Outline each blood parasite and name the species.
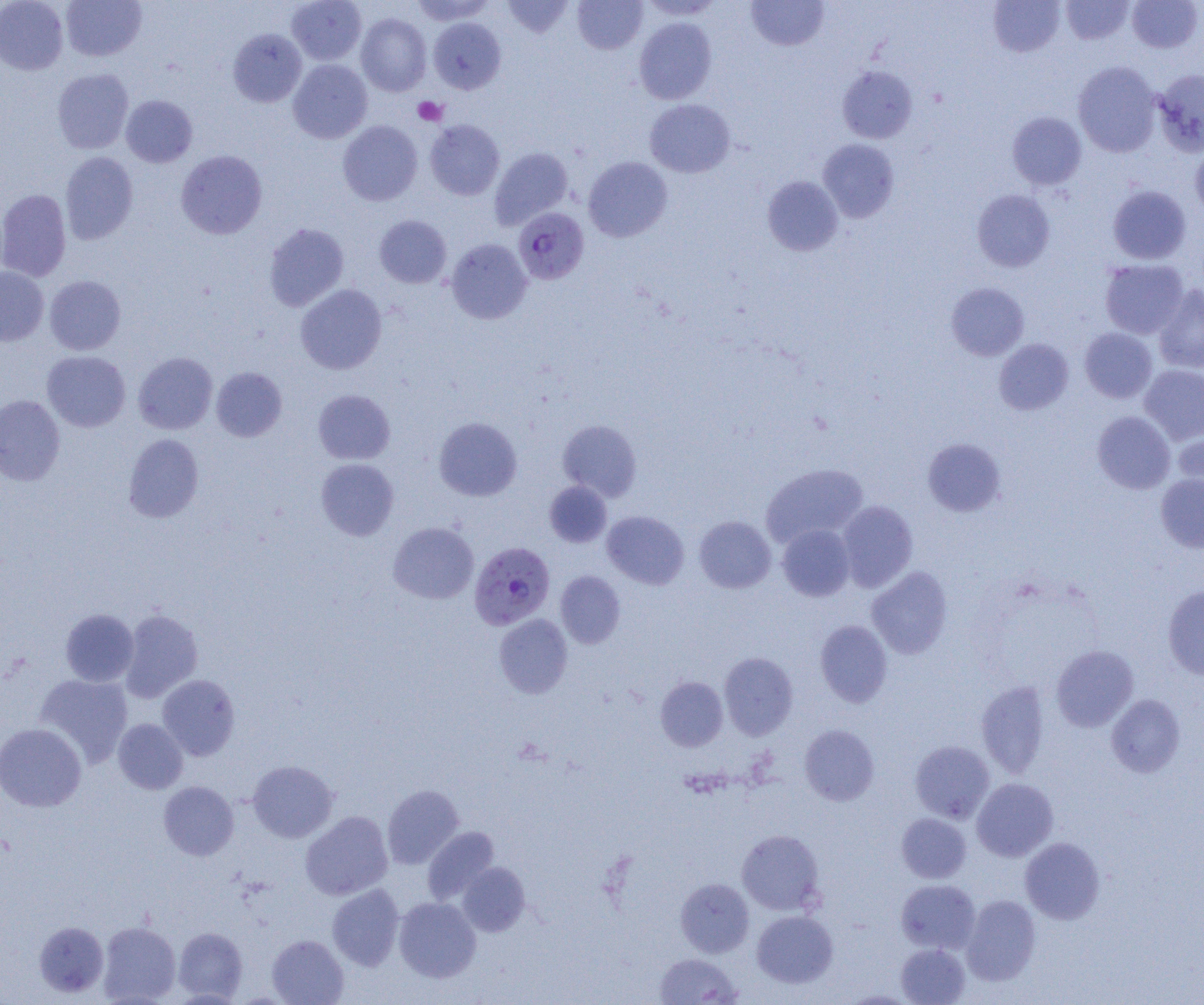
Approximate bounding boxes as (x1, y1, x2, y2) in pixels.
Plasmodium falciparum-infected red blood cells: (513, 208, 589, 285), (469, 542, 555, 629).
No Plasmodium ovale, Plasmodium malariae, Plasmodium vivax, Babesia divergens, or Trypanosoma brucei observed.

slide_level_diagnosis: Plasmodium falciparum
preparation: thin blood smear
magnification: 1000x
platelet_locations: 'approximate bounding boxes as (x1, y1, x2, y2) in pixels: (413, 96, 447, 126)'
modality: light microscopy
field_of_view: one of a larger specimen
image_size: 1204×1005 pixels
uninfected_red_blood_cell_locations: 'approximate bounding boxes as (x1, y1, x2, y2) in pixels: (0, 0, 68, 75), (61, 0, 147, 61), (287, 0, 366, 65), (410, 0, 495, 25), (502, 0, 573, 39), (573, 0, 647, 54), (639, 0, 723, 20), (746, 0, 828, 51), (988, 0, 1065, 58), (1127, 0, 1202, 52), (1061, 1, 1134, 44), (356, 13, 432, 96), (634, 16, 716, 105), (428, 17, 505, 94), (228, 28, 307, 107), (288, 59, 372, 143), (1072, 61, 1162, 157), (837, 66, 917, 144), (53, 68, 133, 154), (1154, 68, 1204, 156), (121, 95, 197, 167), (645, 99, 735, 178), (1007, 111, 1086, 190), (425, 119, 504, 200), (338, 120, 423, 206), (818, 139, 899, 222), (1190, 143, 1204, 220), (489, 147, 573, 230), (176, 150, 267, 239), (60, 152, 138, 244), (583, 156, 672, 242), (762, 176, 843, 256), (1107, 185, 1191, 264), (0, 189, 71, 282), (972, 189, 1055, 272), (374, 215, 451, 288), (264, 223, 349, 311), (445, 238, 532, 324), (1100, 259, 1188, 339), (0, 267, 49, 346), (45, 275, 125, 355), (946, 282, 1029, 360), (295, 284, 387, 374), (1153, 285, 1204, 373), (1079, 328, 1157, 403), (994, 339, 1073, 415), (42, 350, 130, 432), (133, 352, 217, 434), (1139, 365, 1204, 444), (211, 367, 287, 442), (313, 389, 395, 464), (0, 395, 65, 485), (1092, 411, 1175, 494), (433, 417, 522, 501), (558, 419, 641, 501), (1174, 425, 1204, 499), (123, 433, 204, 522), (922, 438, 1006, 516), (316, 458, 399, 541), (760, 464, 868, 547), (1156, 474, 1204, 552), (544, 481, 612, 548), (836, 500, 918, 592), (603, 510, 689, 589), (694, 516, 776, 593), (388, 522, 479, 604), (777, 524, 854, 601), (866, 566, 953, 659), (555, 571, 626, 648), (1163, 585, 1204, 679), (60, 609, 139, 686), (119, 609, 203, 702), (494, 614, 573, 698), (815, 620, 892, 707), (1051, 645, 1138, 732), (719, 652, 798, 740), (34, 674, 133, 768), (157, 674, 240, 760), (656, 676, 728, 751), (976, 681, 1050, 778), (1106, 694, 1185, 777), (113, 718, 188, 794), (0, 723, 86, 812), (800, 724, 879, 805), (910, 740, 995, 823), (247, 760, 338, 843), (972, 778, 1058, 861), (158, 781, 239, 860), (382, 784, 464, 869), (301, 811, 393, 900), (896, 813, 971, 883), (422, 826, 499, 904), (737, 829, 825, 915), (1020, 837, 1105, 924), (457, 862, 530, 936), (676, 878, 754, 957), (896, 879, 981, 953), (327, 883, 404, 970), (961, 894, 1041, 985), (394, 897, 480, 982), (751, 910, 838, 988), (34, 921, 108, 997), (97, 921, 180, 1004), (173, 927, 248, 1001), (267, 934, 348, 1005), (896, 943, 970, 1004), (655, 953, 743, 1004)'